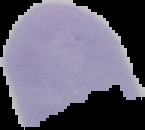

From a thin blood smear. Cell region segmented out of the field of view; the surrounding area is masked to black. Result: Plasmodium parasites detected. Image is 145×130 pixels.